Report the malaria status of this cell.
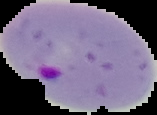

It is parasitized.

The area outside the segmented cell region is set to black. From a thin blood smear. Image is 157×115 pixels.